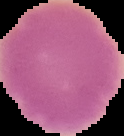

From a thin blood film. Image is 124×136 pixels. Malaria status: uninfected. Segmented cell region on a black background.